Identify the cell.
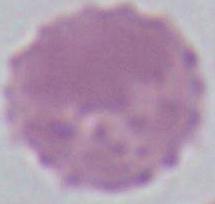

This is an erythrocyte.

Summary:
  - Modality: micrograph
  - Magnification: 1000x